Locate every Plasmodium ovale-infected red blood cell.
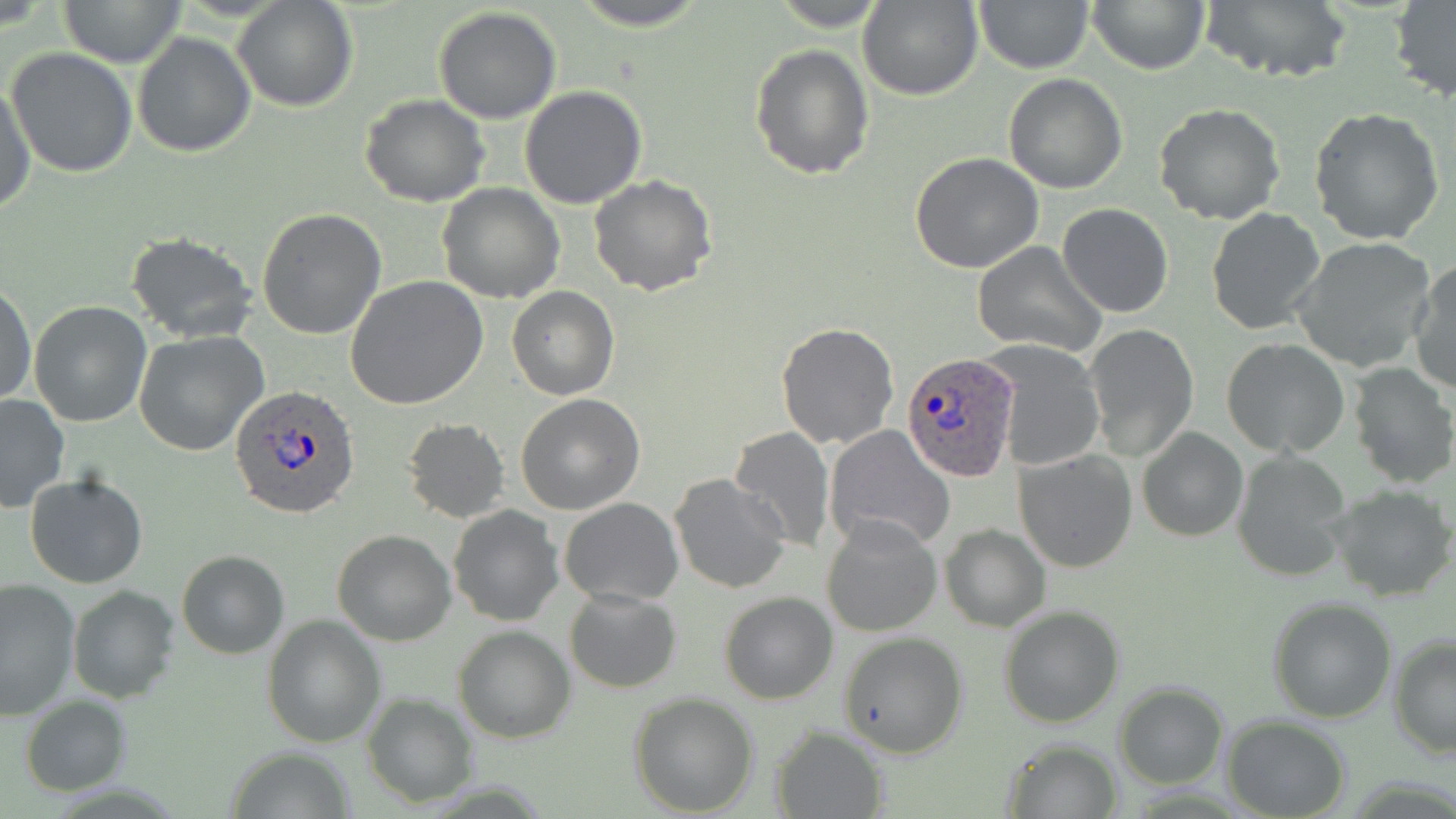

Approximate bounding boxes as (x1, y1, x2, y2) in pixels.
Plasmodium ovale-infected red blood cells: (902, 353, 1019, 481), (231, 385, 361, 519).

slide-level diagnosis = Plasmodium ovale
modality = light microscopy
image size = 1456×819 pixels
field of view = single
magnification = 1000x
uninfected red blood cell locations = approximate bounding boxes as (x1, y1, x2, y2) in pixels: (60, 0, 188, 68), (570, 0, 711, 31), (973, 0, 1092, 73), (1088, 0, 1210, 73), (1197, 0, 1355, 86), (232, 1, 359, 112), (858, 1, 983, 101), (1389, 2, 1456, 102), (432, 8, 562, 124), (132, 32, 256, 157), (749, 44, 874, 179), (6, 47, 138, 178), (1003, 72, 1127, 193), (0, 80, 36, 217), (519, 86, 649, 210), (359, 94, 489, 207), (1155, 102, 1287, 224), (1308, 108, 1446, 248), (911, 153, 1044, 273), (588, 175, 718, 296), (436, 182, 565, 302), (1058, 203, 1173, 318), (256, 208, 387, 340), (1206, 208, 1325, 335), (125, 231, 258, 344), (1292, 238, 1435, 371), (971, 242, 1105, 356), (1408, 261, 1456, 396), (345, 275, 488, 410), (0, 283, 36, 406), (506, 285, 620, 399), (29, 300, 153, 428), (775, 322, 899, 450), (1086, 324, 1199, 460), (134, 331, 266, 455), (1222, 338, 1349, 457), (985, 341, 1104, 472), (1347, 363, 1455, 489), (515, 394, 644, 515), (0, 395, 69, 514), (402, 418, 511, 523), (823, 425, 957, 554), (725, 427, 834, 552), (1136, 428, 1249, 544), (1015, 448, 1139, 573), (1232, 450, 1353, 582), (26, 472, 147, 589), (668, 473, 791, 595), (1330, 484, 1454, 602), (559, 497, 683, 606), (448, 505, 563, 625), (822, 517, 942, 637), (939, 525, 1049, 631), (332, 528, 456, 645), (176, 550, 288, 659), (0, 579, 80, 720), (66, 584, 180, 703), (564, 588, 682, 694), (718, 592, 838, 704), (1268, 596, 1398, 722), (998, 606, 1125, 729), (262, 613, 385, 747), (452, 626, 574, 743), (838, 633, 968, 757), (1388, 635, 1456, 758), (1114, 682, 1228, 789), (363, 692, 479, 806), (628, 692, 760, 816), (20, 696, 131, 796), (1223, 716, 1350, 818), (770, 725, 888, 819), (999, 738, 1123, 818), (222, 746, 358, 819)
stain = May-Grünwald-Giemsa
preparation = thin blood film